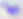
Summary:
  - Magnification: 400x
  - Identification: Toxoplasma gondii
  - Modality: micrograph